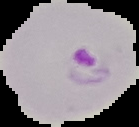
{
  "image_type": "segmented cell region on a black background",
  "image_size": "139×127 pixels",
  "preparation": "thin blood film",
  "result": "malaria parasites detected"
}